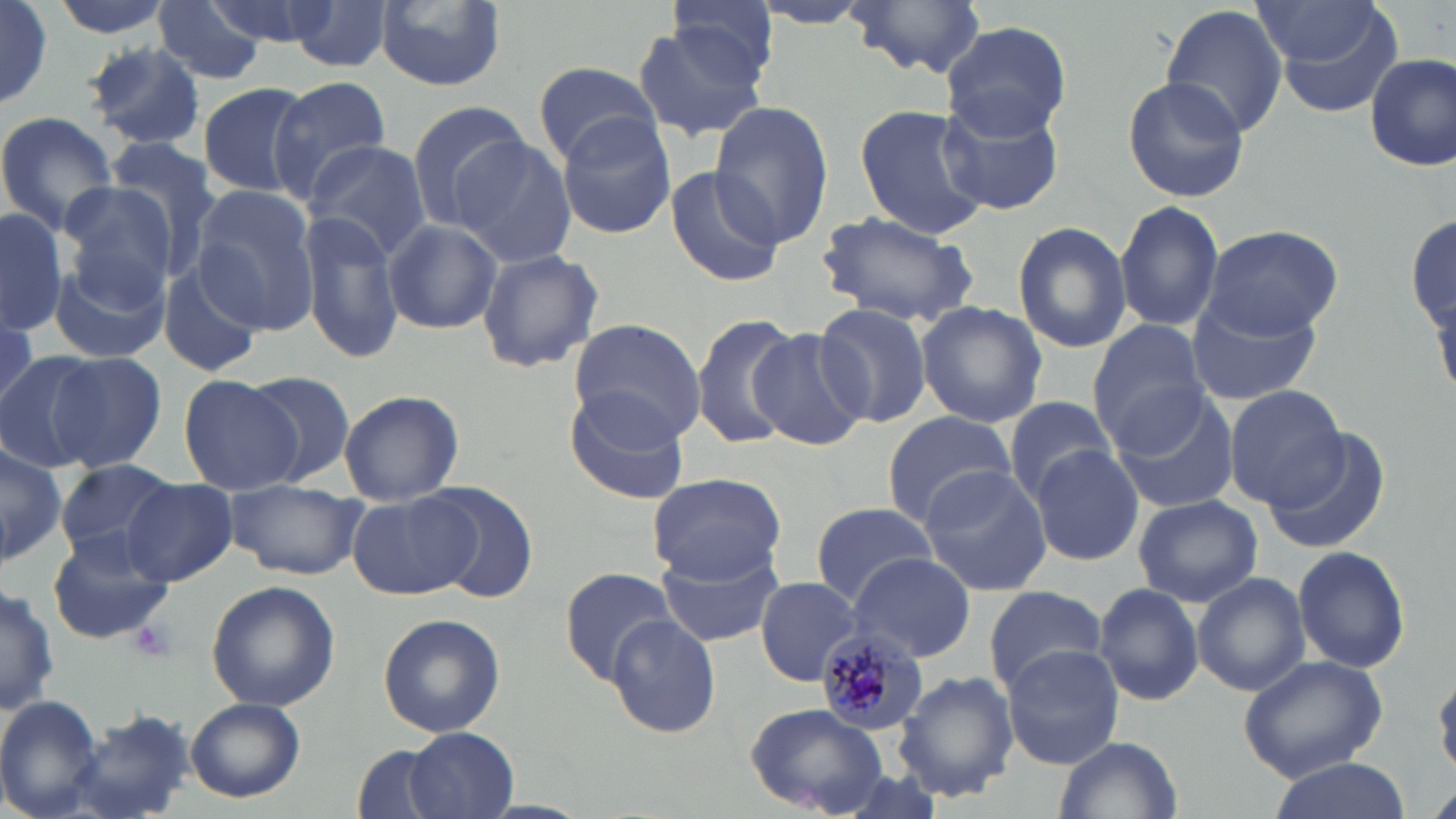 Approximate bounding boxes as [x1, y1, x2, y2] in pixels. Uninfected red blood cell locations: [47, 0, 175, 38], [206, 0, 336, 48], [376, 0, 506, 91], [750, 0, 881, 29], [287, 1, 397, 74], [846, 1, 986, 76], [1161, 2, 1288, 140], [0, 3, 54, 110], [151, 3, 266, 86], [664, 3, 779, 96], [1253, 4, 1384, 64], [1269, 8, 1406, 119], [941, 21, 1072, 139], [631, 23, 767, 139], [82, 41, 206, 151], [1365, 52, 1456, 170], [532, 61, 663, 164], [266, 74, 394, 202], [1122, 76, 1250, 204], [196, 81, 317, 199], [940, 98, 1063, 216], [402, 99, 532, 231], [708, 101, 836, 250], [852, 103, 991, 239], [0, 112, 123, 235], [556, 115, 678, 239], [453, 136, 579, 268], [101, 140, 222, 272], [302, 141, 435, 262], [661, 166, 785, 290], [54, 181, 184, 302], [191, 186, 324, 334], [1113, 198, 1224, 331], [0, 207, 67, 334], [301, 211, 406, 364], [812, 211, 982, 327], [1405, 216, 1455, 330], [381, 218, 502, 335], [1012, 221, 1132, 355], [1202, 223, 1345, 338], [477, 246, 604, 375], [48, 253, 173, 366], [156, 265, 264, 379], [1184, 290, 1323, 407], [814, 300, 934, 429], [916, 301, 1047, 428], [692, 315, 802, 450], [566, 319, 707, 443], [1085, 321, 1210, 451], [747, 327, 869, 451], [46, 350, 167, 470], [0, 351, 104, 473], [243, 370, 359, 489], [177, 374, 302, 494], [1224, 384, 1348, 506], [562, 388, 691, 504], [336, 389, 466, 504], [1109, 390, 1239, 514], [1003, 397, 1118, 500], [882, 408, 1018, 528], [1262, 429, 1389, 553], [0, 439, 65, 570], [1030, 449, 1143, 566], [52, 460, 174, 559], [919, 466, 1054, 594], [647, 471, 789, 585], [121, 480, 238, 586], [225, 480, 365, 581], [424, 483, 540, 604], [348, 492, 479, 600], [1133, 494, 1259, 608], [804, 502, 943, 606], [46, 529, 176, 646], [1292, 544, 1411, 673], [657, 548, 784, 648], [847, 553, 977, 662], [558, 567, 676, 686], [1192, 572, 1309, 695], [756, 576, 864, 685], [205, 580, 339, 712], [0, 582, 59, 718], [1094, 582, 1204, 707], [982, 585, 1109, 698], [377, 612, 506, 737], [606, 612, 721, 739], [1002, 645, 1123, 768], [1238, 654, 1388, 779], [895, 671, 1019, 802], [0, 695, 108, 819], [186, 698, 306, 802], [744, 705, 892, 817], [62, 710, 195, 819], [404, 726, 521, 819], [1054, 734, 1183, 819], [350, 744, 456, 819], [1263, 758, 1410, 817]. Platelet locations: [129, 618, 178, 663]. Plasmodium malariae-infected red blood cell locations: [816, 627, 931, 733]. Slide-level diagnosis: Plasmodium malariae. Single field of view. Light microscopy. Thin blood smear. Captured at 1000x magnification. Image is 1456×819 pixels. May-Grünwald-Giemsa-stained preparation.